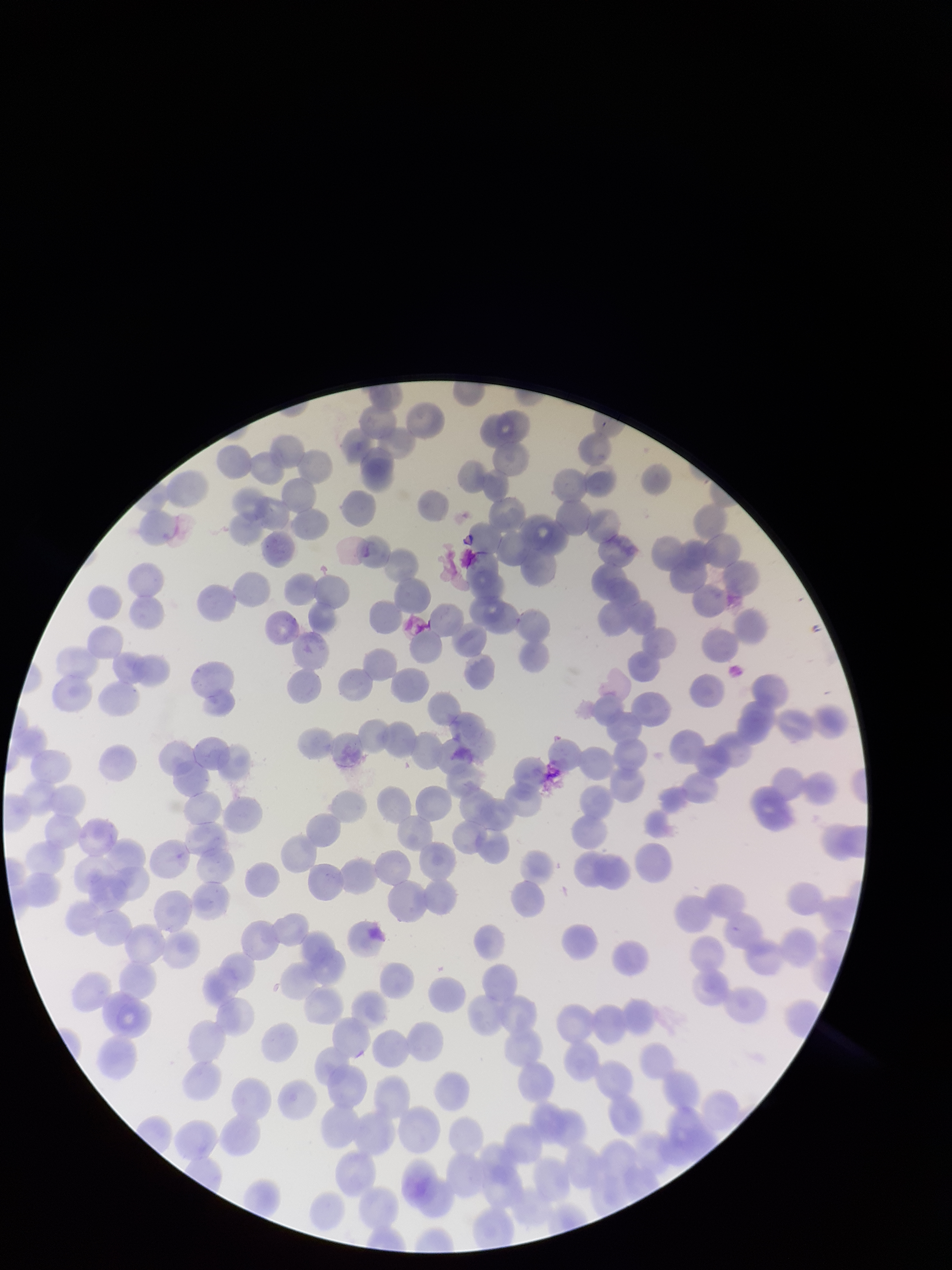
Parasitized red blood cell count: 0. Species reported for this patient: Plasmodium falciparum. Photographed through the microscope eyepiece with a smartphone camera. Giemsa stain. Red blood cell count: 208. Patient malaria status: positive. Single field of view. Image is 952×1270 pixels. Preparation: thin blood smear. Parasitized red blood cells: none identified.